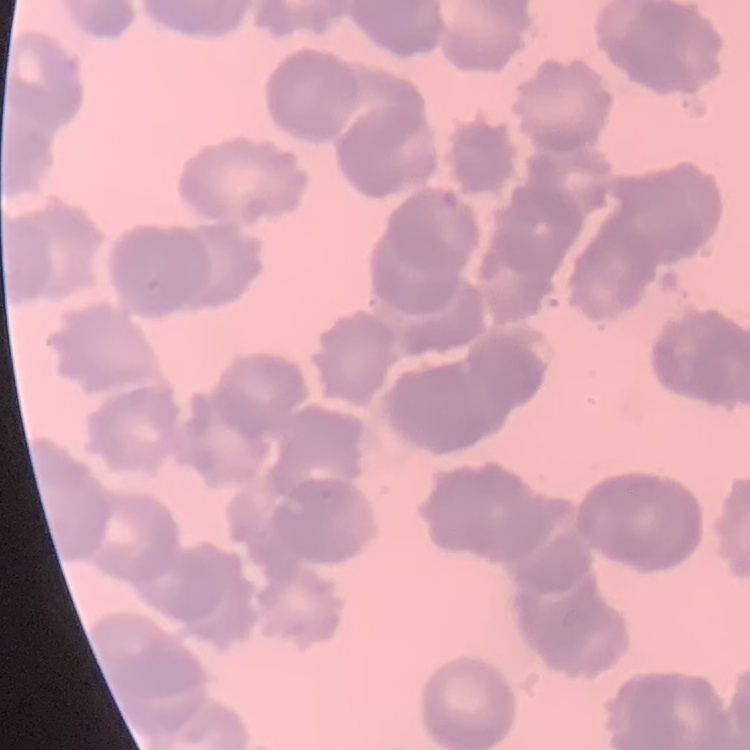
The erythrocytes exhibit rouleaux formation. Field's or Giemsa stain. Square crop of a larger photomicrograph. Thin blood smear.